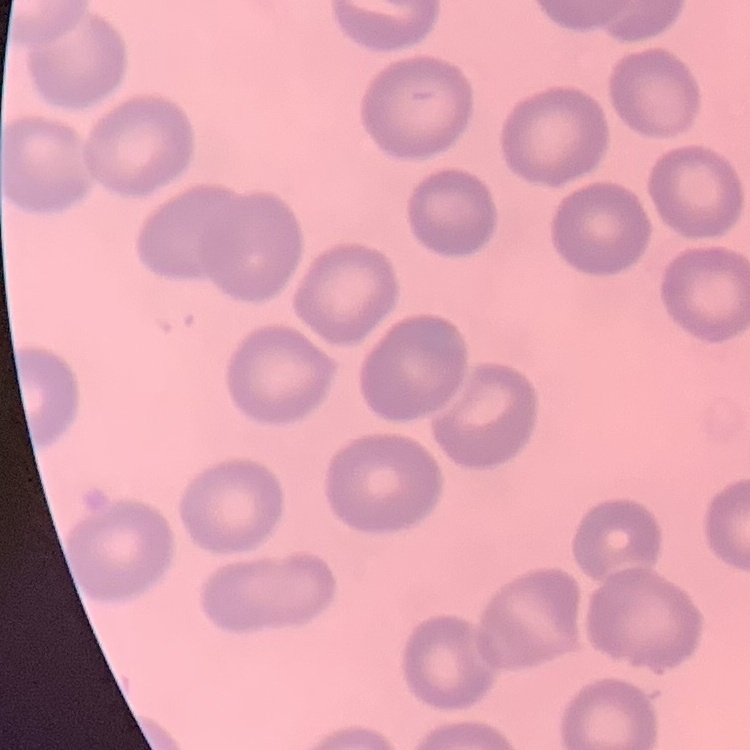
red blood cell morphology = no rouleaux formation
image type = square crop of a larger photomicrograph
preparation = thin blood smear
stain = Field's or Giemsa